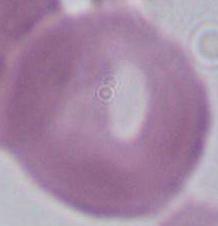

modality = micrograph
identification = red blood cell
magnification = 1000x